Classify this cell by malaria status.
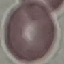
It is uninfected.

Summary:
  - Stain: Giemsa
  - Image type: cell patch, automatically extracted from a larger field of view and resized to 64 × 64 pixels
  - Preparation: thin blood film
  - Capture: smartphone through the microscope eyepiece